Report the malaria status of this cell.
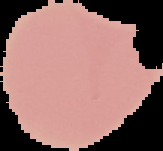
Uninfected.

image_type: segmented cell region with the area outside set to black
preparation: thin blood film
image_size: 163×151 pixels